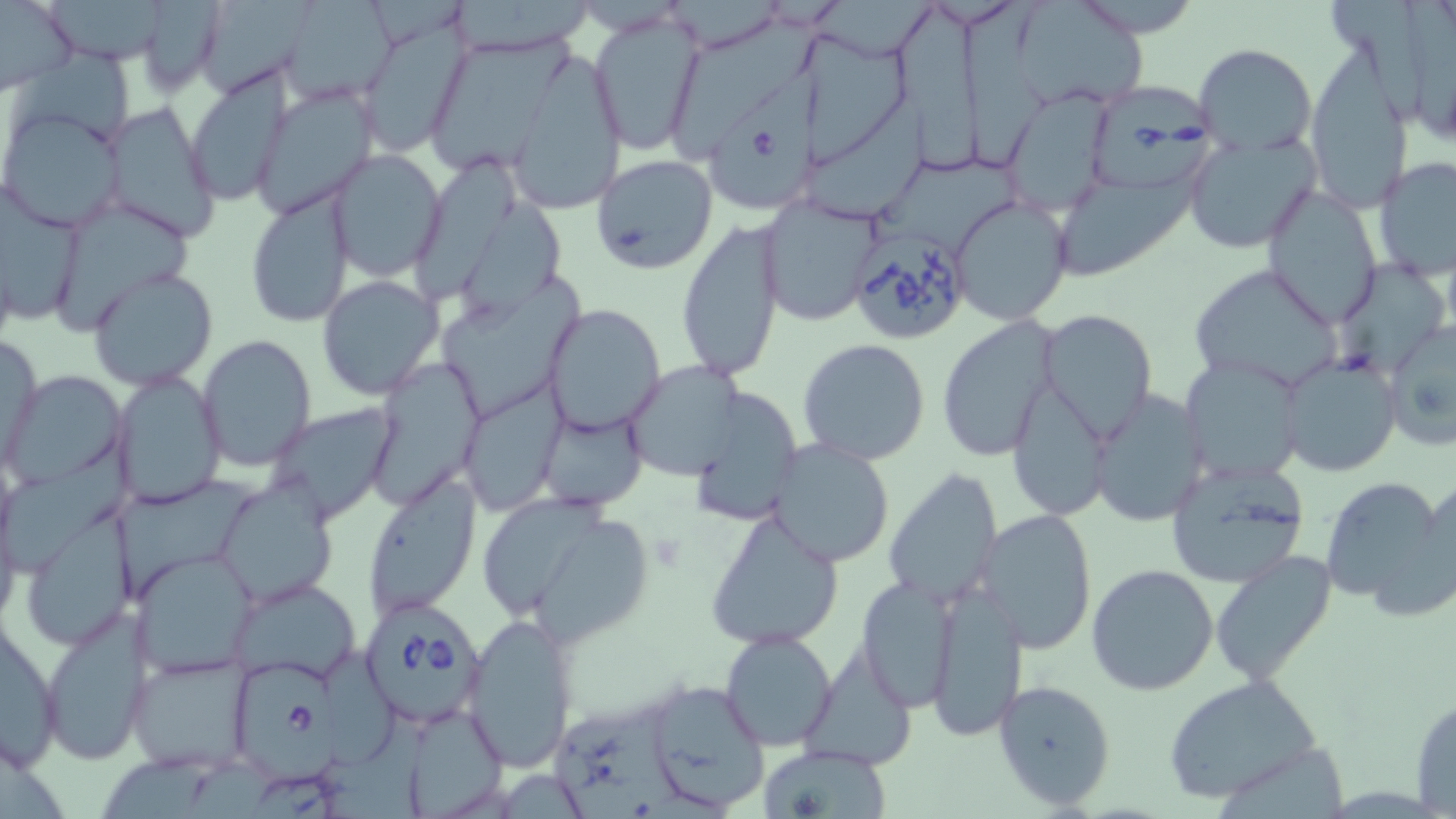

slide-level diagnosis = Babesia divergens
preparation = thin blood film
uninfected red blood cell locations = approximate bounding boxes as (x1,y1)-(x2,y2) corner pairs in pixels: (0,0)-(77,94), (48,0)-(175,66), (197,0)-(320,105), (1020,0)-(1150,110), (1329,0)-(1435,126), (281,1)-(399,105), (1411,2)-(1456,145), (956,3)-(1057,173), (891,4)-(992,173), (589,10)-(704,157), (673,18)-(833,163), (355,20)-(468,159), (433,35)-(586,176), (799,37)-(921,160), (8,38)-(140,146), (1194,43)-(1316,156), (509,56)-(633,220), (1303,56)-(1411,212), (183,69)-(291,206), (254,88)-(378,218), (998,88)-(1119,214), (808,98)-(940,221), (96,102)-(222,244), (0,108)-(125,232), (1183,131)-(1321,254), (328,150)-(448,281), (418,153)-(520,299), (591,154)-(718,276), (879,154)-(1030,242), (1374,157)-(1456,279), (1054,174)-(1200,278), (1261,183)-(1384,328), (1,185)-(84,330), (245,186)-(354,328), (952,195)-(1073,327), (52,197)-(200,338), (464,197)-(572,324), (760,197)-(885,325), (675,221)-(785,381), (1339,256)-(1442,378), (1185,264)-(1342,390), (88,268)-(218,390), (444,271)-(589,414), (317,274)-(445,399), (543,304)-(666,436), (935,314)-(1061,460), (1039,317)-(1152,440), (1382,317)-(1456,452), (2,333)-(45,466), (197,334)-(317,473), (797,339)-(932,465), (1180,355)-(1307,484), (1279,355)-(1399,477), (367,358)-(481,505), (623,362)-(744,482), (113,369)-(226,510), (3,371)-(124,487), (1007,383)-(1113,518), (688,387)-(803,522), (464,389)-(562,514), (1089,389)-(1211,527), (264,401)-(403,525), (538,405)-(646,510), (0,436)-(137,583), (768,441)-(895,568), (1165,461)-(1311,587), (883,469)-(1003,610), (121,471)-(276,601), (364,471)-(483,619), (1319,474)-(1453,612), (217,479)-(338,605), (478,492)-(650,639), (27,503)-(137,652), (705,505)-(844,651), (983,509)-(1098,654), (133,552)-(258,675), (1210,552)-(1336,686), (1085,563)-(1219,697), (856,575)-(960,710), (232,578)-(361,683), (928,582)-(1027,743), (40,610)-(156,764), (462,611)-(581,775), (1,620)-(63,772), (719,629)-(837,751), (802,643)-(916,772), (127,653)-(255,775), (1165,674)-(1326,806), (992,678)-(1118,811), (644,679)-(773,812), (1410,695)-(1456,815), (552,697)-(689,819), (757,744)-(891,817)
magnification = 1000x
modality = light microscopy
Babesia divergens-infected red blood cell locations = approximate bounding boxes as (x1,y1)-(x2,y2) corner pairs in pixels: (696,64)-(831,218), (1089,84)-(1221,194), (847,232)-(970,345), (364,601)-(487,723), (226,657)-(343,772)
stain = May-Grünwald-Giemsa
image size = 1456×819 pixels
field of view = single